Classify this cell by malaria status.
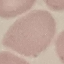

Uninfected.

Photographed with a smartphone camera at the microscope eyepiece. Automatically extracted cell patch, resized to 64 × 64 pixels. Giemsa-stained preparation. Thin blood smear.